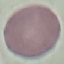 Malaria status: uninfected. Acquired by smartphone through the microscope eyepiece. Automatically extracted cell patch, resized to 64 × 64 pixels. Giemsa-stained preparation. Thin blood smear.